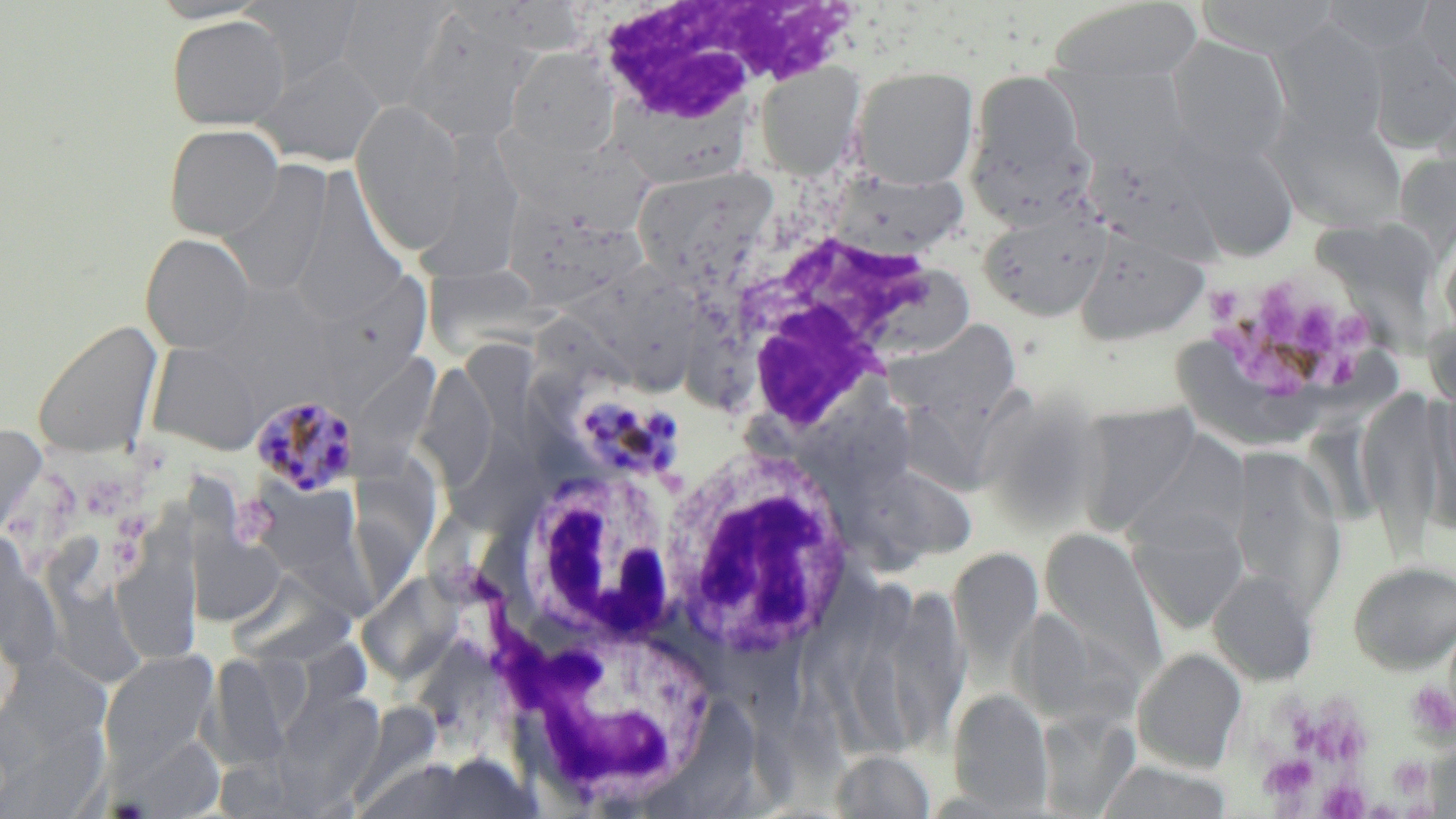
Summary:
  - Coordinate format: approximate bounding boxes as [x1, y1, x2, y2] in pixels
  - Platelet locations: [1204, 269, 1380, 410], [233, 492, 280, 545], [1404, 682, 1455, 744], [1307, 702, 1371, 769], [1258, 754, 1319, 806], [1388, 756, 1433, 798], [1318, 780, 1370, 818]
  - Uninfected red blood cell locations: [239, 0, 366, 90], [1195, 0, 1342, 57], [1417, 0, 1456, 94], [336, 1, 455, 108], [1045, 1, 1206, 84], [404, 10, 535, 146], [166, 15, 290, 130], [1271, 20, 1389, 145], [1167, 36, 1292, 163], [506, 46, 620, 157], [253, 52, 386, 166], [754, 61, 865, 178], [851, 66, 979, 188], [1058, 67, 1189, 171], [965, 70, 1092, 220], [606, 97, 759, 188], [350, 98, 466, 254], [1270, 108, 1409, 234], [429, 116, 530, 285], [164, 123, 284, 240], [504, 131, 661, 233], [1178, 134, 1301, 261], [220, 159, 333, 299], [631, 165, 779, 288], [830, 168, 969, 260], [283, 169, 413, 323], [1308, 200, 1444, 356], [499, 202, 650, 309], [978, 204, 1112, 322], [1074, 228, 1211, 346], [140, 233, 256, 353], [582, 261, 690, 389], [338, 266, 436, 407], [414, 270, 563, 353], [32, 318, 164, 460], [892, 319, 1024, 424], [465, 336, 552, 470], [1174, 340, 1317, 442], [146, 341, 264, 455], [354, 348, 446, 475], [425, 352, 491, 490], [796, 388, 916, 499], [1355, 391, 1446, 555], [889, 392, 1028, 489], [1075, 404, 1205, 537], [445, 420, 551, 536], [0, 425, 46, 541], [1124, 432, 1249, 552], [354, 438, 448, 580], [1228, 445, 1347, 612], [839, 463, 976, 556], [1128, 506, 1249, 633], [126, 510, 206, 666], [187, 525, 288, 627], [47, 526, 135, 686], [1040, 527, 1166, 675], [949, 547, 1042, 673], [1348, 559, 1456, 674], [229, 564, 365, 664], [363, 564, 475, 675], [1208, 569, 1318, 686], [882, 582, 969, 749], [1, 643, 122, 780], [1133, 648, 1247, 773], [99, 650, 219, 772], [204, 651, 294, 771], [275, 686, 385, 806], [949, 689, 1054, 815], [649, 696, 763, 814], [1037, 708, 1139, 816], [110, 733, 226, 818], [830, 749, 937, 818], [1094, 760, 1235, 819]
  - White blood cell locations: [577, 2, 835, 132], [703, 173, 985, 414], [658, 446, 860, 661], [517, 457, 698, 631], [476, 612, 728, 797]
  - Plasmodium malariae-infected red blood cell locations: [568, 389, 687, 486], [250, 392, 360, 497]
  - Slide-level diagnosis: Plasmodium malariae
  - Preparation: thin blood film
  - Image size: 1456×819 pixels
  - Stain: May-Grünwald-Giemsa
  - Magnification: 1000x
  - Field of view: one of a larger specimen
  - Modality: light microscopy